Name the parasite shown.
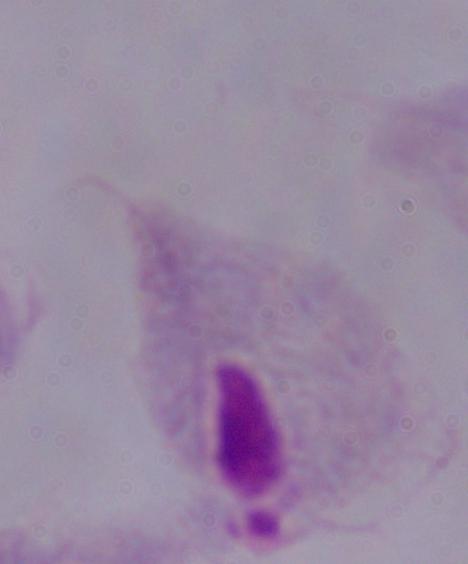

A trichomonad.

Micrograph. Captured at 1000x magnification.